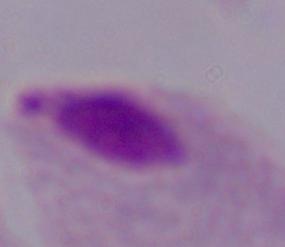
Summary:
  - Identification: trichomonad
  - Magnification: 1000x
  - Modality: photomicrograph